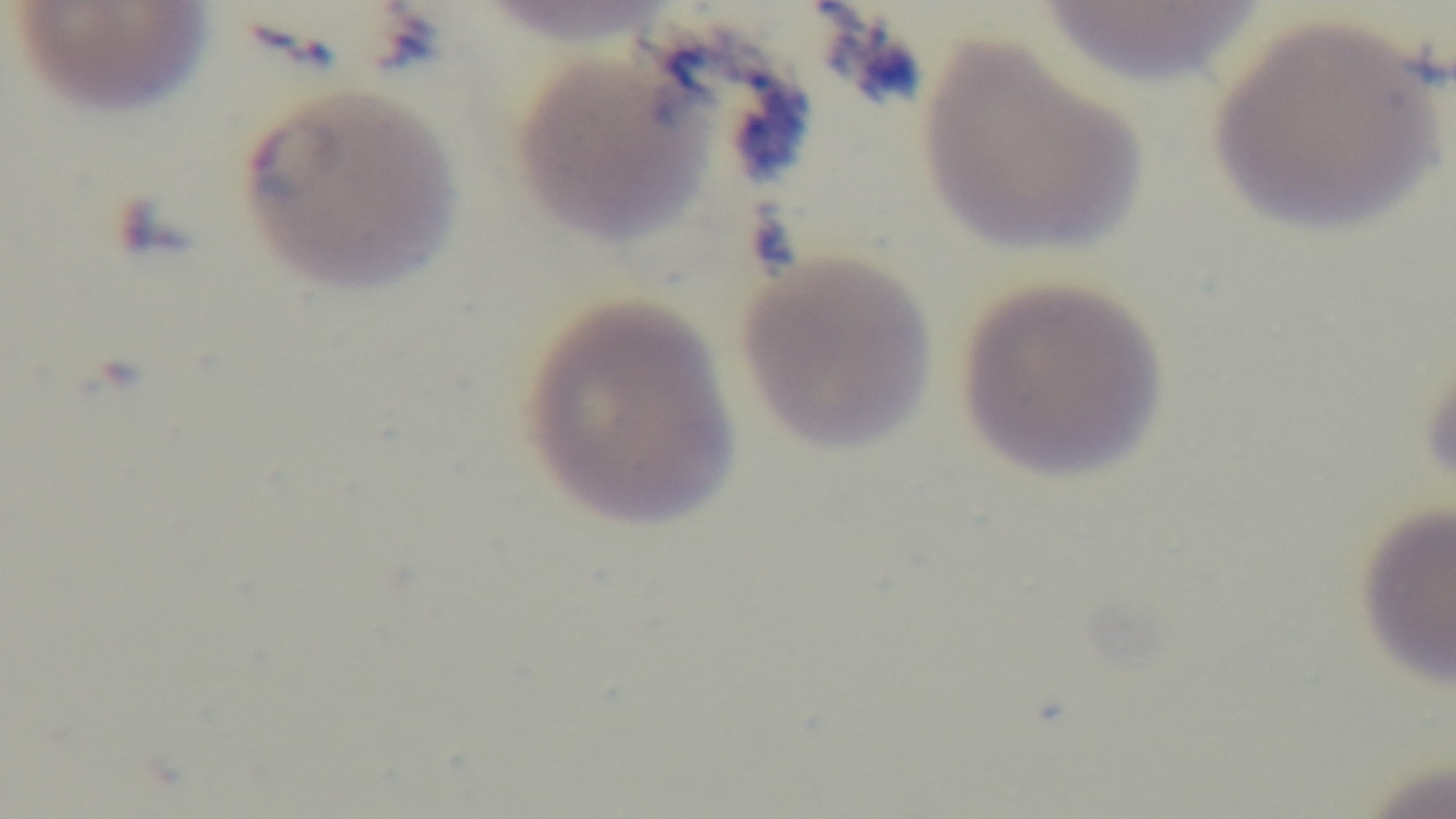

Summary:
  - Preparation: thin smear
  - Modality: light microscopy
  - Malaria status: infected
  - Field of view: single
  - Stain: Giemsa
  - Capture: mounted 4K digital camera
  - Objective: 100x oil immersion